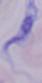 Micrograph. 1000x magnification. A trypanosome is seen.